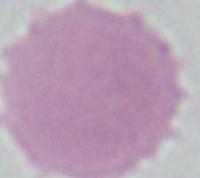
{
  "identification": "erythrocyte",
  "magnification": "1000x",
  "modality": "micrograph"
}